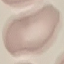
Summary:
  - Malaria status: uninfected
  - Stain: Giemsa
  - Preparation: thin smear
  - Capture: smartphone camera at the microscope eyepiece
  - Image type: cell patch, automatically extracted from a larger field of view and resized to 64 × 64 pixels